Locate every Plasmodium parasite by life-cycle stage, and every leukocyte.
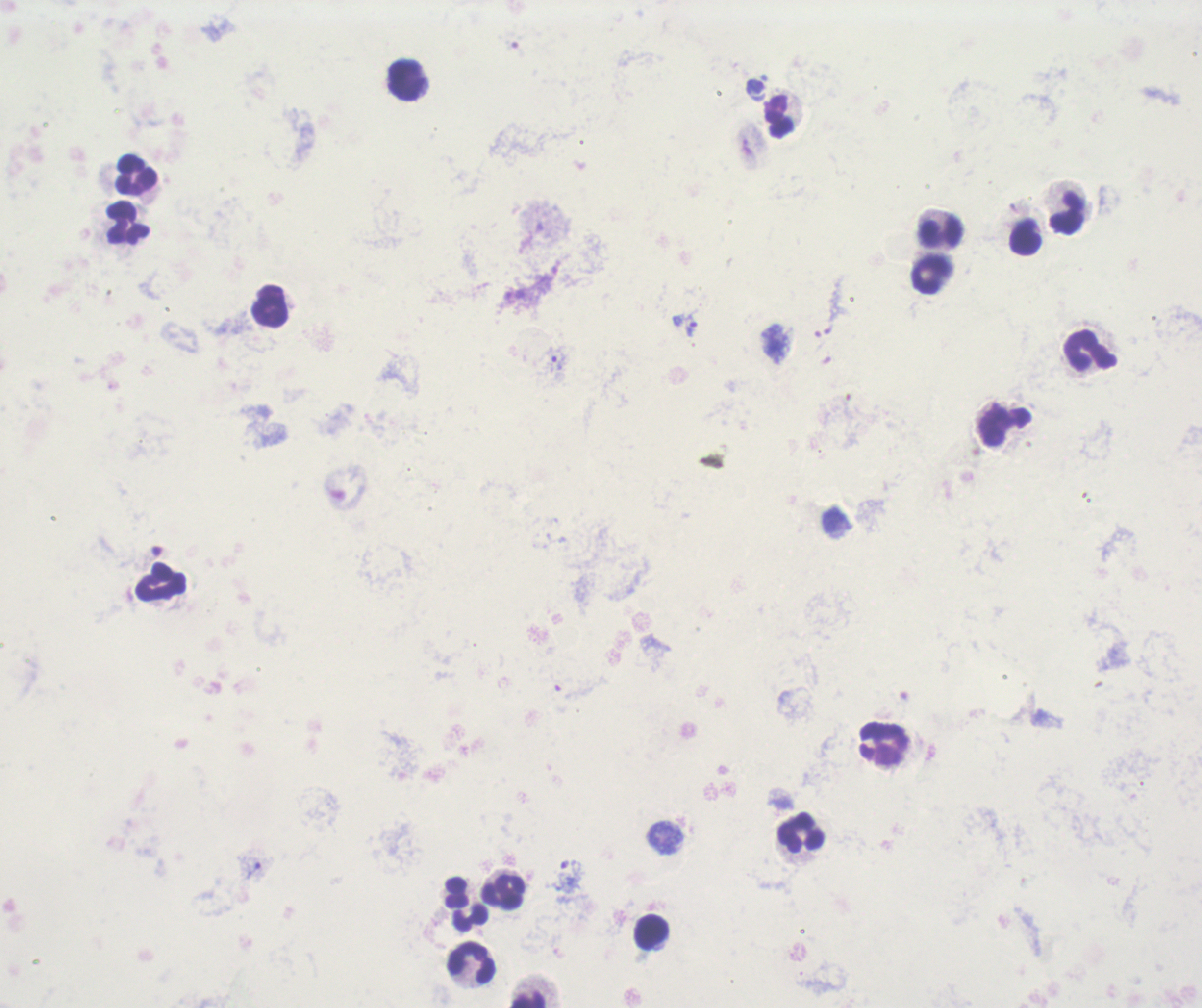
Approximate object centers, in pixels from the top-left corner.
Trophozoites: (x=690, y=322), (x=557, y=358).
No schizont or gametocyte forms observed.
Leukocytes: (x=407, y=81), (x=780, y=117), (x=134, y=176), (x=1067, y=214), (x=126, y=224), (x=941, y=231), (x=1026, y=238), (x=931, y=275), (x=271, y=307), (x=1089, y=351), (x=1004, y=426), (x=160, y=581), (x=884, y=743), (x=802, y=832), (x=504, y=892), (x=651, y=934), (x=471, y=963), (x=527, y=998).

Summary:
  - Preparation: thick smear of blood
  - Stain: Romanowsky
  - Image size: 1202×1008 pixels
  - Context: previously used in an actual diagnosis
  - Magnification: 100x
  - Field of view: single
  - Background quality: poor